Name the cell type shown.
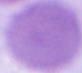
This is an erythrocyte.

1000x magnification. Micrograph.